Classify this cell by malaria status.
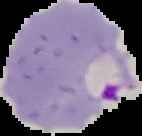

It is parasitized.

preparation = thin blood smear
image type = segmented cell region with the area outside set to black
image size = 142×136 pixels